Identify the parasite.
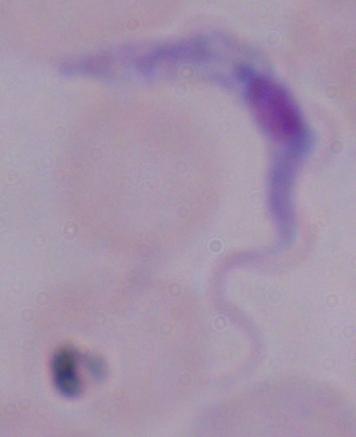

This is a trypanosome.

Summary:
  - Modality: photomicrograph
  - Magnification: 1000x